Name the parasite shown.
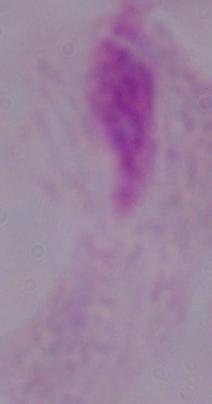
A trichomonad.

{
  "magnification": "1000x",
  "modality": "micrograph"
}